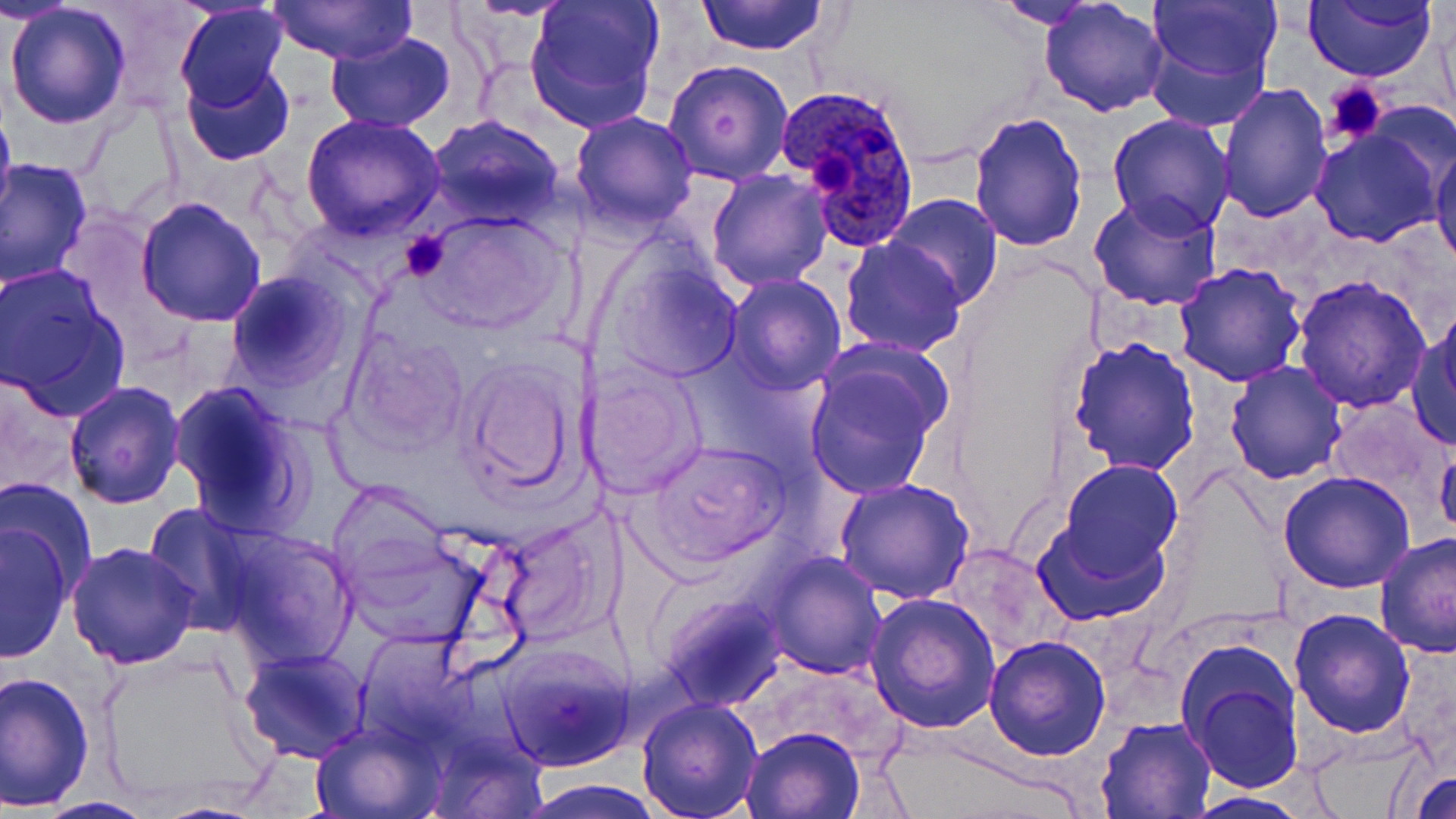 Approximate bounding boxes as [x1, y1, x2, y2] in pixels. Uninfected red blood cell locations: [3, 0, 79, 26], [464, 0, 577, 21], [522, 0, 666, 132], [696, 0, 828, 55], [990, 0, 1108, 29], [1040, 0, 1168, 117], [1143, 0, 1280, 95], [1303, 0, 1438, 82], [270, 1, 417, 64], [5, 4, 131, 129], [174, 6, 290, 113], [325, 31, 456, 130], [663, 59, 793, 186], [182, 61, 295, 167], [1216, 83, 1333, 225], [0, 97, 17, 234], [77, 103, 187, 228], [968, 110, 1089, 252], [569, 111, 699, 233], [1106, 114, 1235, 238], [300, 115, 447, 242], [427, 116, 564, 227], [1308, 126, 1443, 247], [1430, 136, 1456, 271], [1, 158, 94, 289], [706, 170, 832, 292], [1090, 191, 1225, 312], [882, 195, 1005, 308], [135, 197, 266, 327], [415, 212, 568, 337], [839, 236, 967, 356], [600, 249, 745, 384], [1173, 262, 1308, 387], [0, 263, 130, 415], [226, 270, 351, 391], [723, 274, 846, 395], [1291, 274, 1431, 413], [1409, 319, 1456, 449], [342, 328, 471, 454], [1068, 335, 1200, 474], [804, 355, 945, 500], [460, 357, 585, 498], [1224, 360, 1348, 484], [580, 362, 707, 498], [64, 381, 185, 509], [168, 381, 312, 535], [1329, 397, 1453, 514], [1435, 438, 1456, 542], [642, 439, 792, 565], [1057, 459, 1182, 576], [1279, 471, 1417, 592], [1, 477, 98, 596], [834, 478, 975, 605], [325, 479, 454, 591], [137, 502, 265, 633], [490, 515, 616, 643], [1033, 516, 1171, 624], [0, 523, 74, 660], [218, 531, 358, 669], [1374, 531, 1455, 658], [338, 532, 493, 652], [66, 540, 200, 670], [943, 545, 1060, 657], [765, 553, 887, 679], [864, 591, 1001, 734], [660, 596, 781, 710], [1288, 608, 1417, 738], [984, 633, 1110, 759], [498, 642, 633, 772], [238, 647, 370, 763], [100, 651, 267, 811], [1179, 652, 1305, 793], [1, 669, 96, 810], [636, 697, 763, 819], [1097, 716, 1216, 817], [310, 720, 442, 818], [741, 727, 864, 818], [929, 756, 1090, 819], [1408, 769, 1456, 818], [522, 780, 663, 817], [1183, 791, 1314, 818], [37, 796, 156, 818]. Platelet locations: [1324, 80, 1387, 145], [805, 146, 857, 196], [401, 229, 453, 281]. Plasmodium ovale-infected red blood cell locations: [778, 83, 925, 252]. Slide-level diagnosis: Plasmodium ovale. Captured at 1000x magnification. Single field of view. Light microscopy. Image is 1456×819 pixels. May-Grünwald-Giemsa-stained preparation. Thin blood smear.